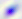
identification = Toxoplasma gondii
modality = photomicrograph
magnification = 400x